Classify this cell by malaria status.
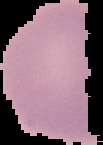
It is uninfected.

image_type: segmented cell region with the area outside set to black
image_size: 103×145 pixels
preparation: thin blood smear